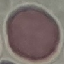
Summary:
  - Result: negative for malaria parasites
  - Stain: Giemsa
  - Capture: smartphone camera at the microscope eyepiece
  - Preparation: thin blood smear
  - Image type: cell patch, automatically extracted from a larger field of view and resized to 64 × 64 pixels